Classify this cell by malaria status.
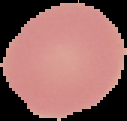
Uninfected.

image size = 127×121 pixels
image type = segmented cell region on a black background
preparation = thin blood film